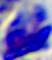

{
  "identification": "white blood cell",
  "modality": "micrograph",
  "magnification": "400x"
}